Comment on the morphology of the red blood cells.
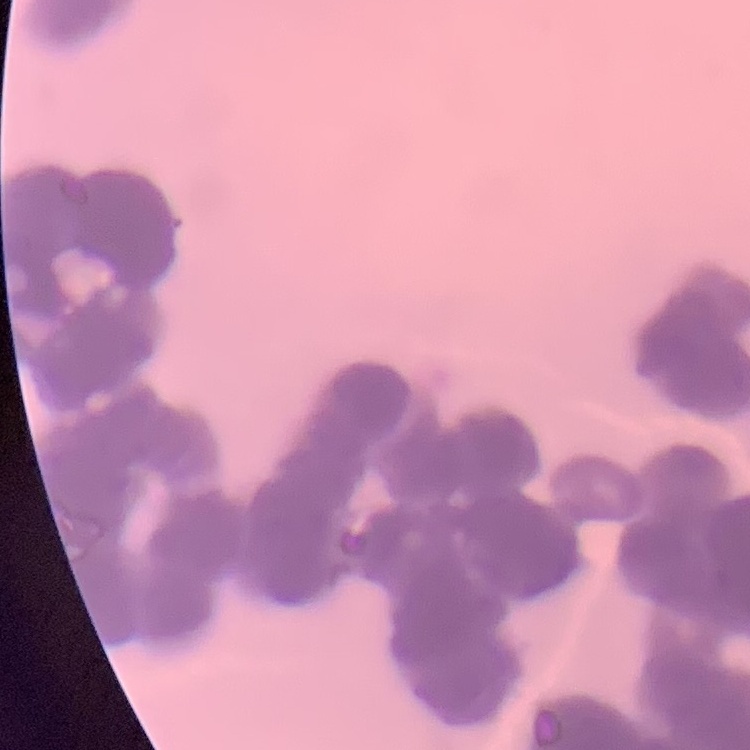
Rouleaux formation.

Summary:
  - Stain: Field's or Giemsa
  - Image type: one tile cut from a larger photomicrograph
  - Preparation: thin peripheral smear